Identify the parasite.
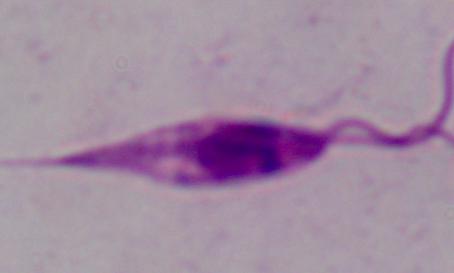

Leishmania.

1000x magnification. Micrograph.